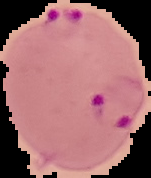
The area outside the segmented cell region is set to black. From a thin blood film. Result: Plasmodium parasites detected. Image is 151×178 pixels.